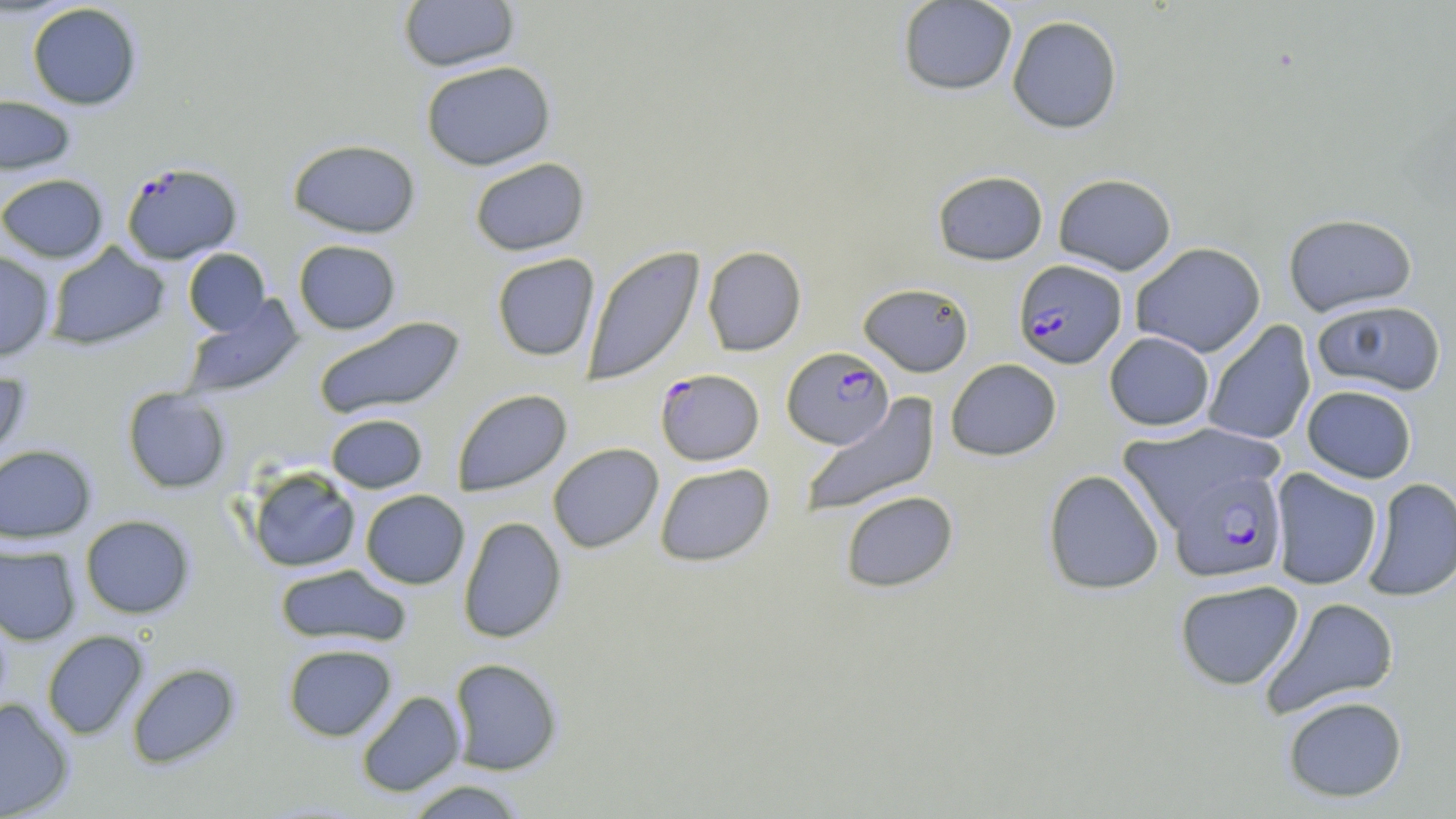
Summary:
  - Coordinate format: approximate bounding boxes as (x1,y1)-(x2,y2) corner pairs in pixels
  - Uninfected red blood cell locations: (397,0)-(520,72), (897,0)-(1017,96), (26,3)-(142,110), (1007,15)-(1123,134), (420,60)-(556,170), (0,93)-(78,175), (288,138)-(421,238), (469,157)-(590,256), (932,170)-(1049,265), (0,173)-(109,262), (1053,173)-(1177,275), (1283,212)-(1417,316), (293,239)-(402,334), (1130,242)-(1266,357), (45,243)-(170,350), (582,246)-(705,386), (702,246)-(807,356), (183,248)-(270,336), (0,251)-(56,361), (491,253)-(599,361), (858,282)-(974,376), (180,294)-(304,400), (1312,299)-(1446,396), (314,316)-(465,419), (1203,320)-(1316,446), (1104,332)-(1214,431), (945,358)-(1062,461), (0,365)-(31,464), (1302,384)-(1417,483), (123,387)-(232,493), (452,389)-(572,496), (800,393)-(940,518), (325,413)-(428,493), (1117,422)-(1283,532), (548,443)-(664,553), (0,444)-(97,544), (654,463)-(775,566), (246,466)-(361,573), (1269,468)-(1382,590), (1042,469)-(1164,595), (1362,477)-(1456,602), (360,490)-(469,589), (840,490)-(958,593), (80,514)-(196,618), (458,516)-(567,643), (0,544)-(81,646), (274,564)-(411,647), (1174,579)-(1304,690), (1262,596)-(1400,718), (42,630)-(149,740), (282,643)-(397,741), (449,658)-(563,775), (126,662)-(241,768), (356,690)-(466,797), (1282,695)-(1408,803), (0,697)-(74,819), (403,779)-(529,818)
  - Plasmodium falciparum-infected red blood cell locations: (121,161)-(242,264), (1013,259)-(1127,369), (781,347)-(894,448), (655,369)-(764,465), (1171,469)-(1286,582)
  - Slide-level diagnosis: Plasmodium falciparum
  - Field of view: single
  - Image size: 1456×819 pixels
  - Magnification: 1000x
  - Stain: May-Grünwald-Giemsa
  - Preparation: thin blood smear
  - Modality: optical microscopy